Look for parasitized red blood cells.
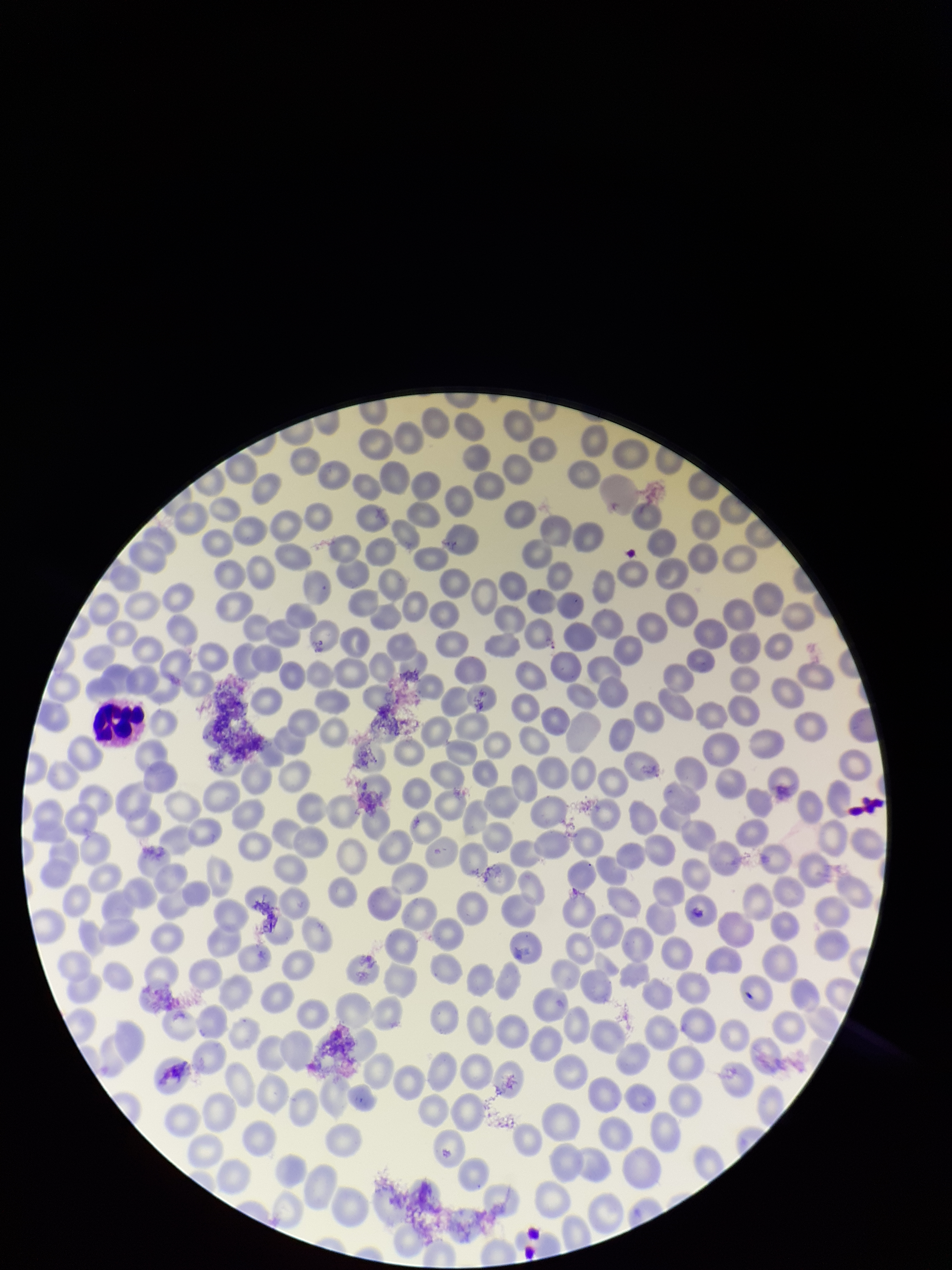

None identified.

Stained with Giemsa. Red blood cell count: 240. One field from this slide. Image is 952×1270 pixels. Patient malaria status: negative. Photographed through the microscope eyepiece with a smartphone camera. Preparation: thin blood smear. Parasitized red blood cell count: 0.